Look for Plasmodium parasites.
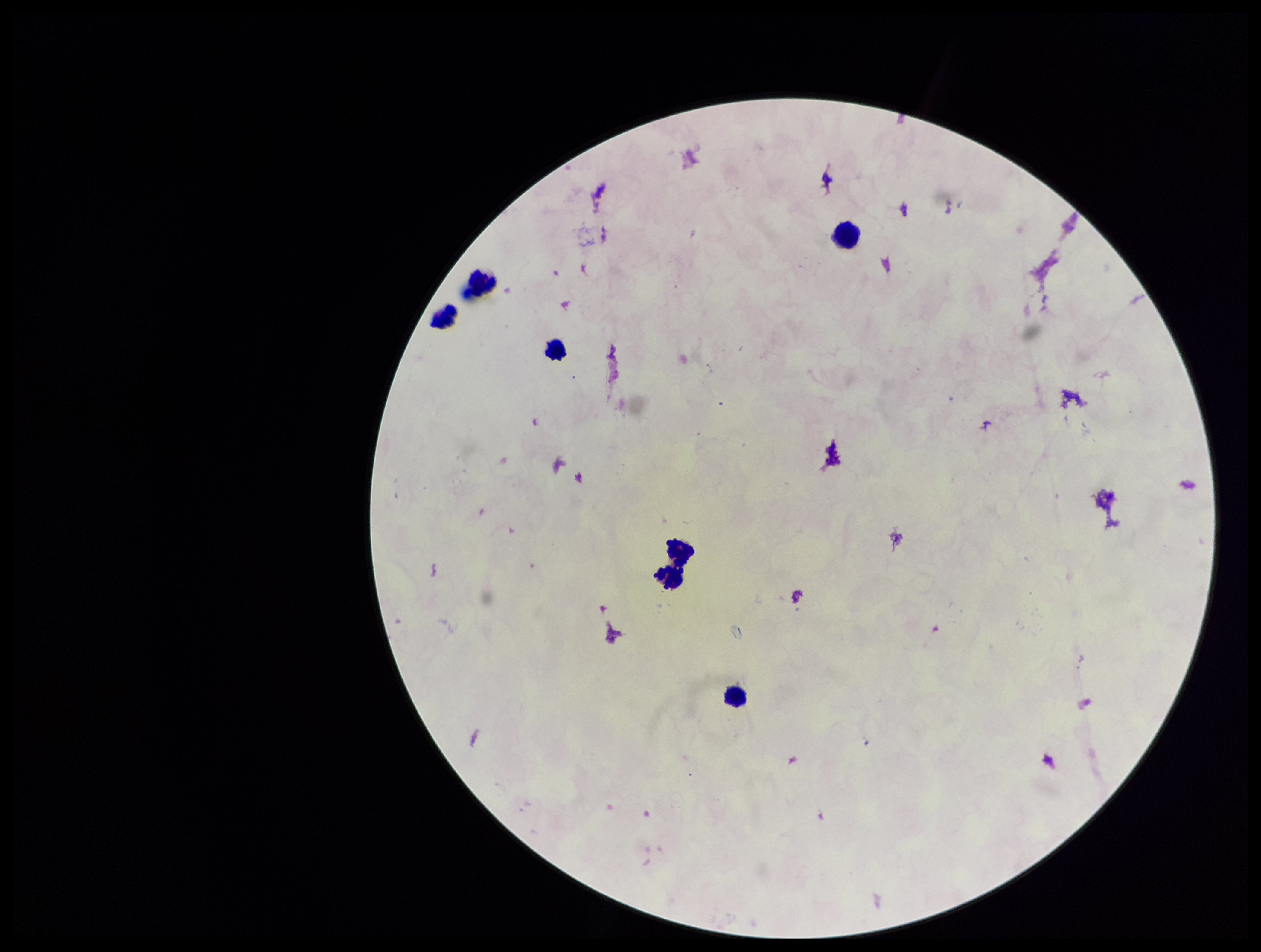

None seen.

leukocyte_count: 6
patient_malaria_status: negative
preparation: thick
image_size: 1261×952 pixels
stain: Giemsa
capture: smartphone photograph through the microscope eyepiece
field_of_view: single
parasite_count: 0